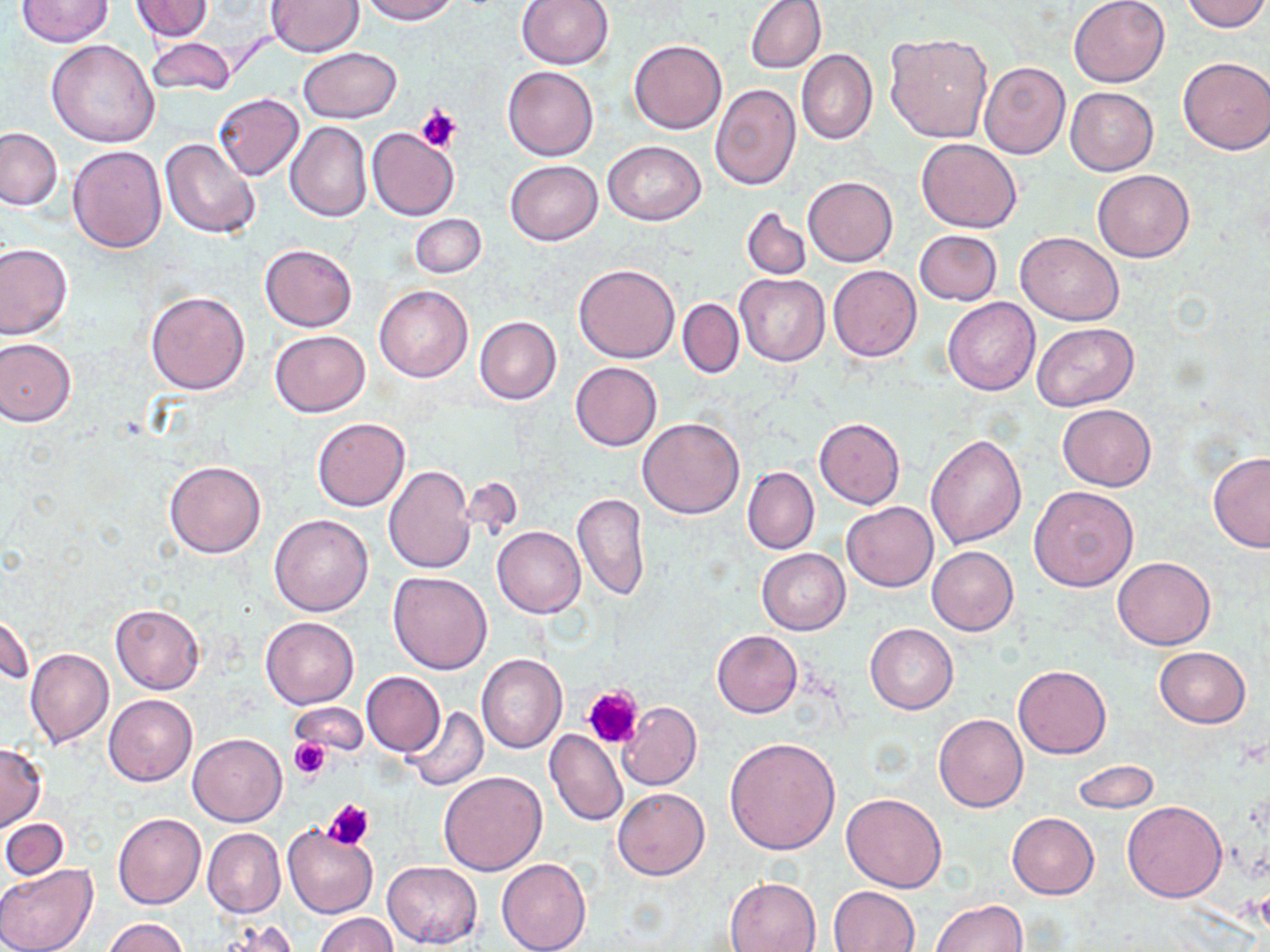 Approximate bounding boxes as [x1, y1, x2, y2] in pixels. Platelet locations: [414, 104, 462, 152], [583, 685, 643, 748], [290, 737, 329, 778], [325, 799, 375, 848]. Uninfected red blood cell locations: [132, 0, 215, 41], [265, 0, 363, 57], [359, 0, 459, 24], [517, 0, 614, 68], [745, 0, 826, 74], [1068, 0, 1170, 87], [1180, 0, 1269, 32], [16, 1, 114, 46], [885, 31, 994, 143], [144, 37, 237, 98], [46, 39, 161, 146], [629, 39, 726, 135], [298, 47, 401, 123], [797, 49, 877, 144], [1178, 55, 1270, 155], [978, 60, 1070, 159], [502, 66, 599, 160], [672, 68, 772, 193], [710, 83, 800, 189], [1066, 87, 1158, 175], [213, 93, 303, 180], [285, 121, 371, 222], [1, 127, 63, 210], [367, 128, 459, 220], [160, 138, 260, 238], [916, 138, 1023, 232], [602, 141, 707, 225], [67, 145, 166, 253], [505, 160, 603, 246], [1092, 171, 1195, 262], [803, 176, 898, 266], [742, 207, 812, 279], [409, 213, 488, 278], [915, 229, 1002, 305], [1016, 232, 1124, 325], [0, 243, 73, 339], [260, 243, 357, 331], [574, 263, 679, 363], [828, 265, 922, 361], [735, 274, 829, 368], [374, 285, 472, 382], [145, 290, 250, 395], [943, 297, 1040, 395], [676, 298, 745, 377], [474, 316, 561, 405], [1033, 323, 1138, 411], [270, 330, 370, 417], [0, 338, 76, 425], [570, 362, 662, 450], [1057, 403, 1157, 491], [312, 417, 409, 511], [638, 417, 745, 518], [814, 417, 905, 509], [925, 432, 1027, 548], [1208, 453, 1270, 552], [165, 461, 266, 559], [383, 464, 475, 575], [743, 466, 819, 555], [1029, 485, 1139, 592], [572, 493, 649, 599], [842, 502, 938, 592], [269, 514, 373, 616], [493, 527, 584, 617], [927, 546, 1018, 636], [757, 549, 850, 634], [1112, 557, 1215, 650], [387, 572, 493, 674], [110, 603, 204, 693], [1, 606, 35, 690], [260, 616, 359, 709], [866, 623, 957, 716], [712, 630, 803, 717], [1155, 646, 1250, 728], [25, 648, 114, 748], [476, 653, 568, 753], [1012, 664, 1112, 758], [361, 671, 445, 756], [104, 694, 198, 787], [617, 701, 702, 791], [289, 703, 369, 758], [401, 706, 489, 791], [933, 714, 1028, 813], [544, 729, 628, 827], [188, 732, 287, 827], [724, 737, 840, 856], [0, 742, 47, 831], [1072, 760, 1159, 814], [438, 771, 547, 875], [612, 787, 710, 881], [841, 793, 947, 893], [1121, 802, 1227, 902], [113, 812, 206, 909], [1006, 812, 1098, 899], [2, 818, 70, 879], [282, 824, 377, 918], [202, 827, 285, 917], [496, 857, 590, 952], [382, 861, 482, 948], [0, 864, 98, 952], [724, 877, 820, 952], [830, 885, 919, 952], [933, 899, 1027, 951], [313, 913, 399, 952], [103, 917, 188, 952], [210, 922, 304, 950]. Slide-level diagnosis: negative for blood parasites. Thin blood smear. Image is 1270×952 pixels. 1000x magnification. May-Grünwald-Giemsa-stained preparation. Light microscopy. One field of a larger specimen.